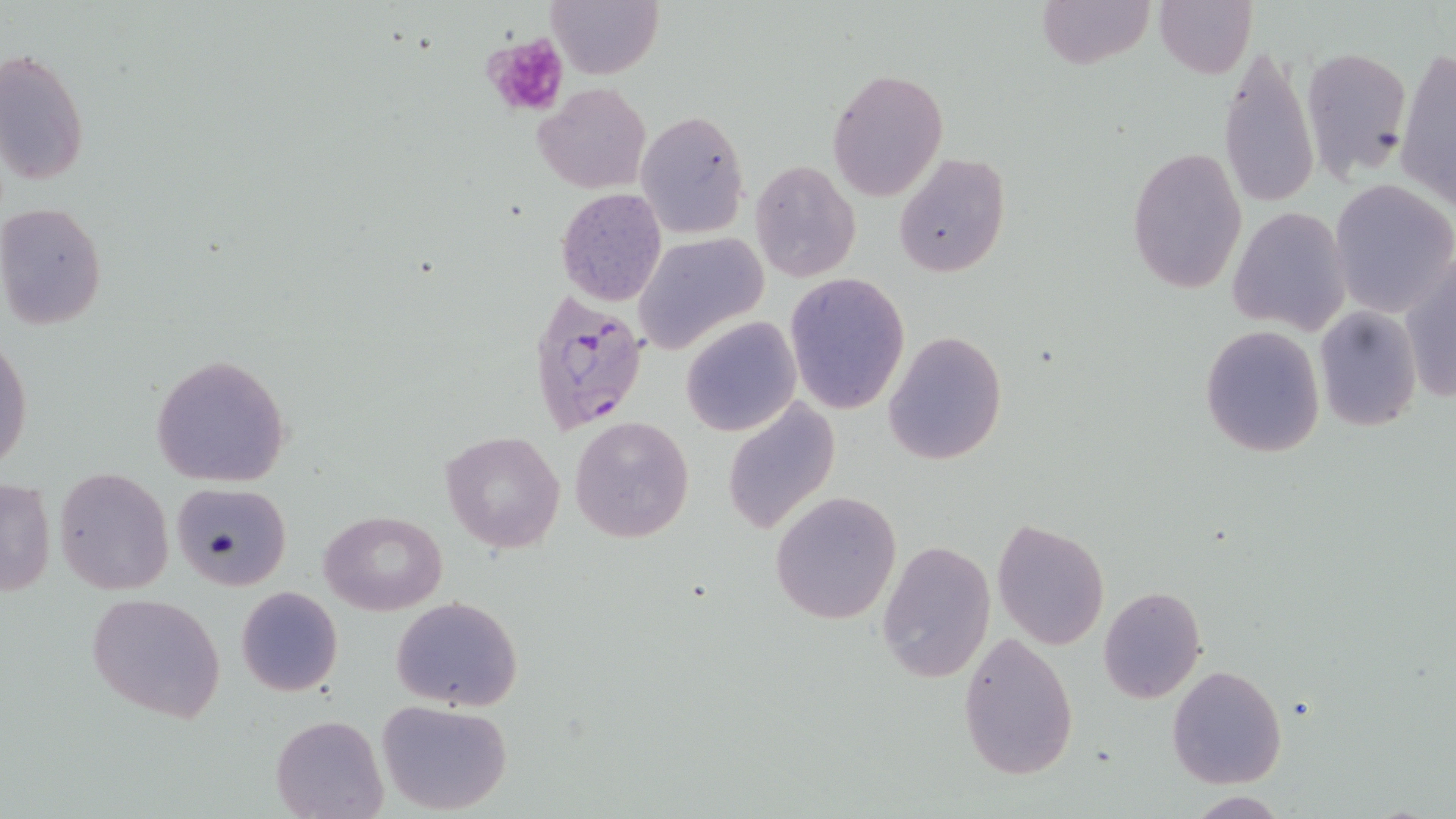

slide-level diagnosis = Plasmodium falciparum
platelet locations = approximate bounding boxes as named x1/y1/x2/y2 corners in pixels: (x1=480, y1=35, x2=569, y2=118)
modality = optical microscopy
image size = 1456×819 pixels
preparation = thin blood smear
Plasmodium falciparum-infected red blood cell locations = approximate bounding boxes as named x1/y1/x2/y2 corners in pixels: (x1=524, y1=291, x2=651, y2=436)
uninfected red blood cell locations = approximate bounding boxes as named x1/y1/x2/y2 corners in pixels: (x1=547, y1=0, x2=664, y2=79), (x1=1036, y1=0, x2=1155, y2=69), (x1=1155, y1=1, x2=1257, y2=79), (x1=1216, y1=40, x2=1318, y2=211), (x1=1300, y1=46, x2=1412, y2=179), (x1=0, y1=48, x2=88, y2=186), (x1=1396, y1=48, x2=1456, y2=210), (x1=826, y1=66, x2=948, y2=202), (x1=532, y1=81, x2=652, y2=192), (x1=635, y1=109, x2=752, y2=239), (x1=1127, y1=145, x2=1248, y2=297), (x1=894, y1=154, x2=1010, y2=276), (x1=751, y1=162, x2=861, y2=281), (x1=1330, y1=179, x2=1455, y2=318), (x1=555, y1=187, x2=669, y2=307), (x1=0, y1=203, x2=107, y2=328), (x1=1228, y1=206, x2=1351, y2=335), (x1=634, y1=233, x2=768, y2=354), (x1=1400, y1=256, x2=1456, y2=404), (x1=784, y1=272, x2=910, y2=414), (x1=1314, y1=304, x2=1422, y2=431), (x1=681, y1=316, x2=801, y2=437), (x1=1199, y1=325, x2=1327, y2=458), (x1=884, y1=330, x2=1007, y2=467), (x1=1, y1=336, x2=33, y2=473), (x1=150, y1=353, x2=293, y2=487), (x1=721, y1=399, x2=840, y2=535), (x1=569, y1=416, x2=694, y2=542), (x1=439, y1=430, x2=566, y2=553), (x1=55, y1=466, x2=173, y2=596), (x1=0, y1=478, x2=55, y2=597), (x1=170, y1=481, x2=293, y2=590), (x1=770, y1=491, x2=902, y2=626), (x1=321, y1=509, x2=449, y2=615), (x1=991, y1=518, x2=1110, y2=651), (x1=878, y1=539, x2=997, y2=684), (x1=235, y1=585, x2=343, y2=697), (x1=1098, y1=585, x2=1206, y2=705), (x1=86, y1=591, x2=225, y2=722), (x1=391, y1=596, x2=524, y2=712), (x1=957, y1=631, x2=1079, y2=782), (x1=1167, y1=665, x2=1286, y2=787), (x1=376, y1=700, x2=514, y2=815), (x1=272, y1=715, x2=387, y2=819), (x1=1182, y1=792, x2=1291, y2=817)
stain = May-Grünwald-Giemsa
magnification = 1000x
field of view = single